Assess the morphology of the red blood cells.
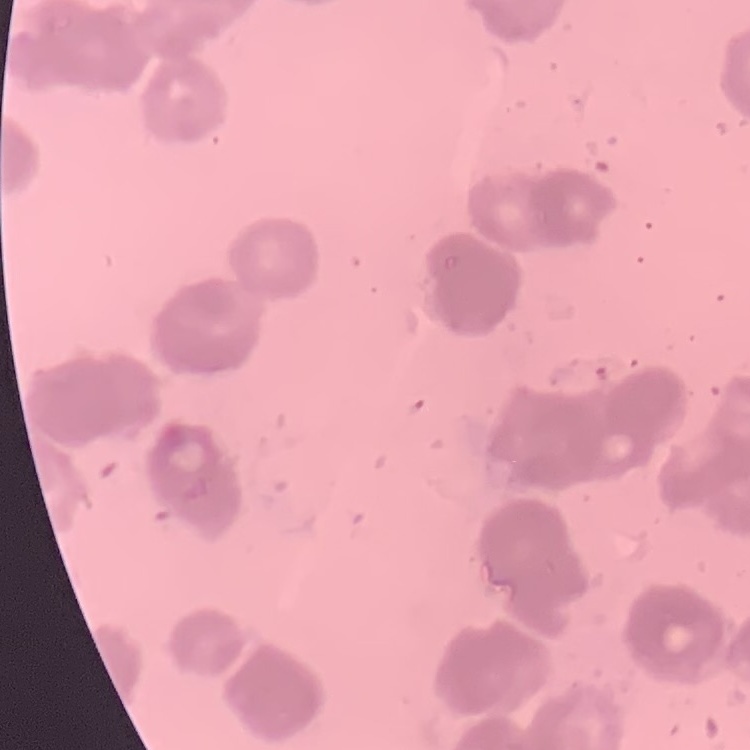

They show rouleaux formation.

image type = one tile cut from a larger photomicrograph
stain = Field's or Giemsa
preparation = thin blood smear